Name the cell type shown.
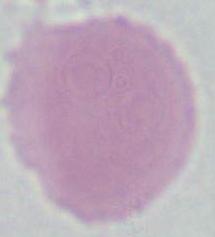

This is an erythrocyte.

Summary:
  - Modality: photomicrograph
  - Magnification: 1000x